Locate every Plasmodium falciparum-infected red blood cell.
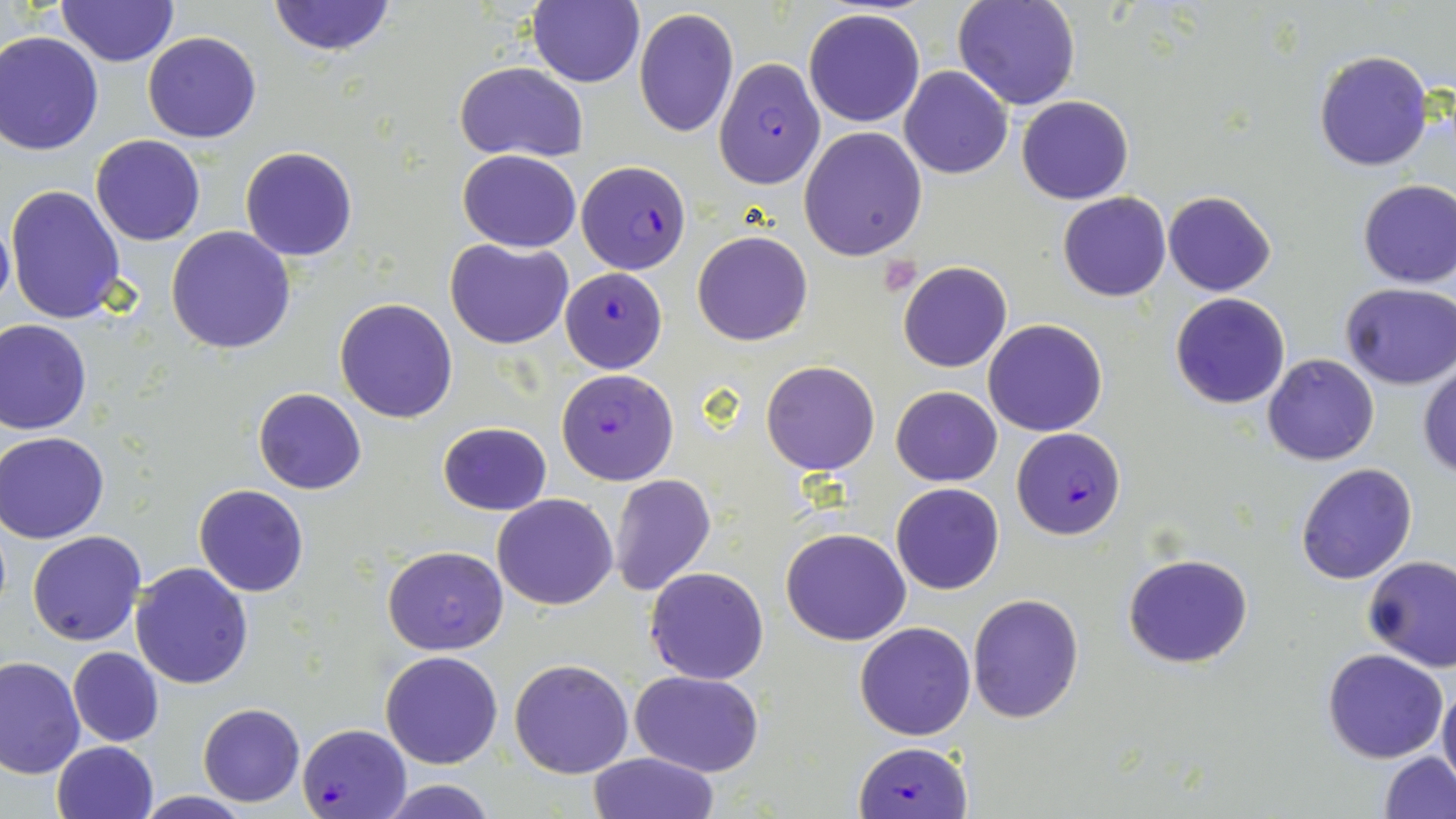

Approximate bounding boxes as (x1,y1)-(x2,y2) corner pairs in pixels.
Plasmodium falciparum-infected red blood cells: (714,58)-(826,189), (579,160)-(690,272), (559,268)-(667,373), (555,368)-(679,485), (1013,427)-(1127,540), (297,723)-(410,817), (855,741)-(972,819).

Summary:
  - Platelet locations: (876,257)-(922,296)
  - Uninfected red blood cell locations: (528,0)-(645,88), (952,0)-(1081,111), (56,1)-(179,67), (266,1)-(399,56), (633,7)-(738,138), (802,9)-(925,128), (0,31)-(104,154), (143,31)-(263,143), (1312,50)-(1435,172), (453,62)-(588,162), (898,66)-(1013,179), (1016,94)-(1134,205), (798,126)-(927,261), (90,134)-(206,246), (239,147)-(359,261), (457,149)-(580,252), (1357,178)-(1456,289), (5,184)-(126,324), (1163,190)-(1276,297), (1057,191)-(1171,302), (0,215)-(14,317), (167,225)-(296,355), (693,230)-(812,346), (445,238)-(573,349), (897,262)-(1012,372), (1340,284)-(1456,389), (1170,292)-(1291,409), (334,298)-(458,421), (0,319)-(92,434), (984,319)-(1108,437), (1262,354)-(1380,466), (761,360)-(881,475), (1418,360)-(1456,478), (891,385)-(1002,486), (253,388)-(368,494), (438,421)-(550,515), (1,430)-(113,542), (1296,463)-(1418,585), (609,474)-(716,596), (890,482)-(1004,595), (193,484)-(309,597), (493,494)-(618,609), (154,512)-(289,663), (782,528)-(911,645), (26,531)-(145,645), (382,545)-(508,655), (1122,552)-(1254,668), (1361,554)-(1456,672), (130,562)-(254,688), (644,567)-(768,684), (967,593)-(1084,723), (855,622)-(976,740), (68,647)-(163,746), (1321,648)-(1451,764), (380,649)-(503,769), (0,654)-(85,778), (509,658)-(634,778), (630,670)-(765,778), (1437,681)-(1456,794), (198,702)-(304,805), (51,740)-(159,819), (1378,750)-(1456,818), (586,752)-(720,819), (374,778)-(499,818), (132,792)-(257,819)
  - Slide-level diagnosis: Plasmodium falciparum
  - Magnification: 1000x
  - Preparation: thin blood film
  - Modality: optical microscopy
  - Field of view: one of a larger specimen
  - Stain: May-Grünwald-Giemsa
  - Image size: 1456×819 pixels